Identify the parasite.
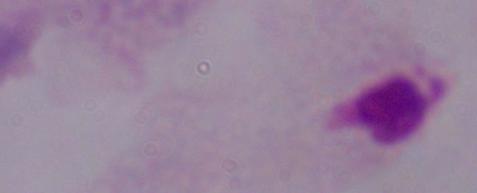

A trichomonad.

Summary:
  - Modality: micrograph
  - Magnification: 1000x